Report the malaria status of this cell.
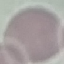
Uninfected.

stain = Giemsa
capture = smartphone camera at the microscope eyepiece
preparation = thin blood smear
image type = automatically extracted cell patch, resized to 64 × 64 pixels